State which parasite is depicted.
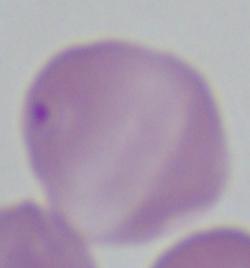

Babesia.

Summary:
  - Modality: photomicrograph
  - Magnification: 1000x